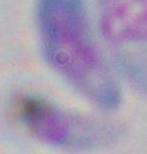 Toxoplasma gondii is shown. Captured at 1000x magnification. Micrograph.